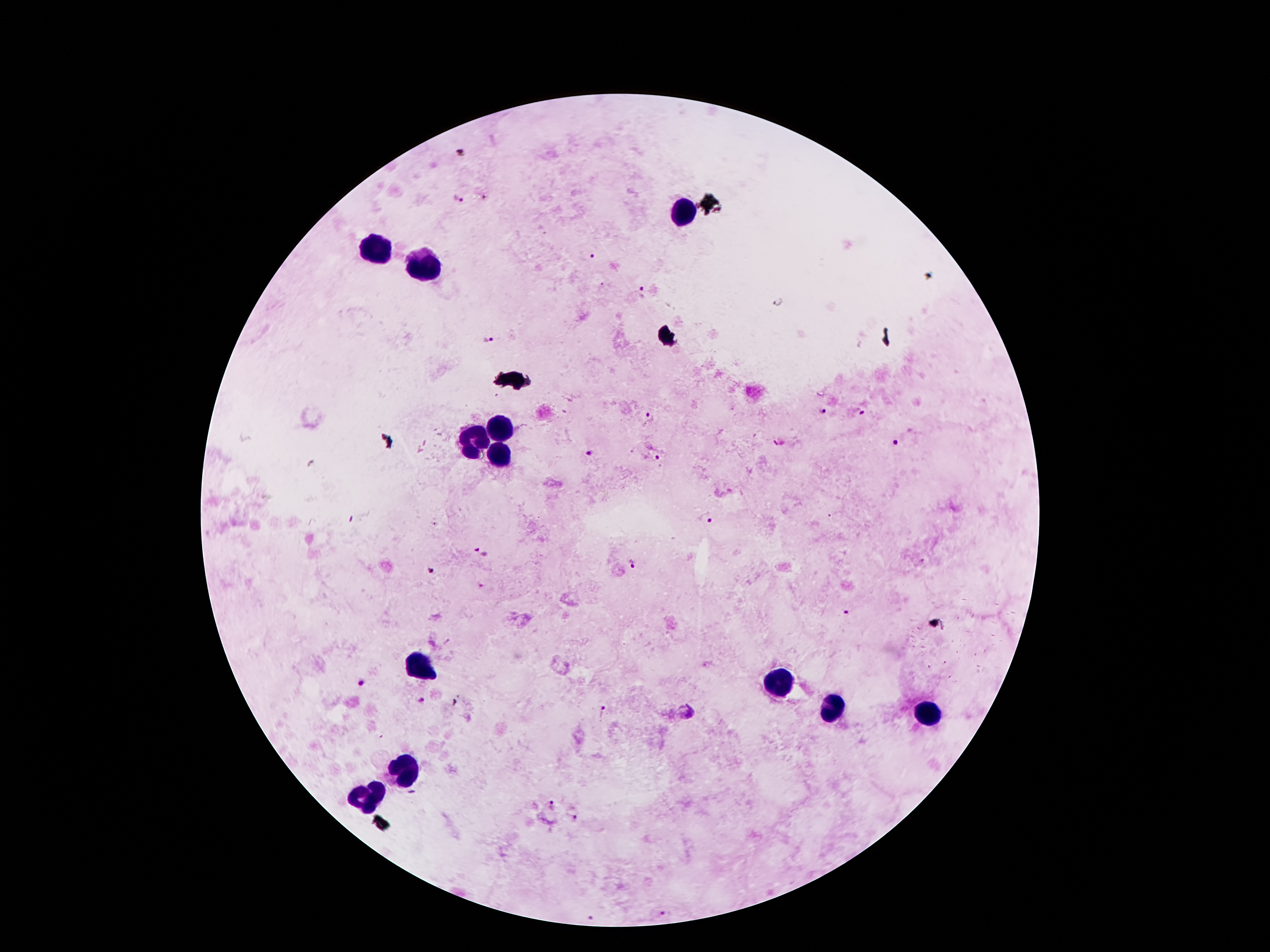

coordinate format = approximate centers as [x, y] in pixels
leukocyte locations = [686, 213], [371, 251], [426, 264], [499, 431], [474, 442], [500, 456], [418, 666], [783, 683], [829, 710], [921, 714], [405, 774], [367, 798]
malaria parasite locations = [457, 198], [592, 257], [643, 295], [490, 339], [824, 411], [862, 412], [650, 416], [900, 441], [591, 452], [654, 457], [706, 518], [481, 551], [633, 564], [432, 570], [847, 613], [361, 684], [423, 702], [603, 713], [551, 804], [574, 817], [667, 914], [591, 918]
preparation = thick peripheral-blood smear
capture = smartphone camera through the microscope eyepiece
field of view = single
stain = Giemsa
image size = 1270×952 pixels
patient malaria status = positive for Plasmodium falciparum
magnification = 100x